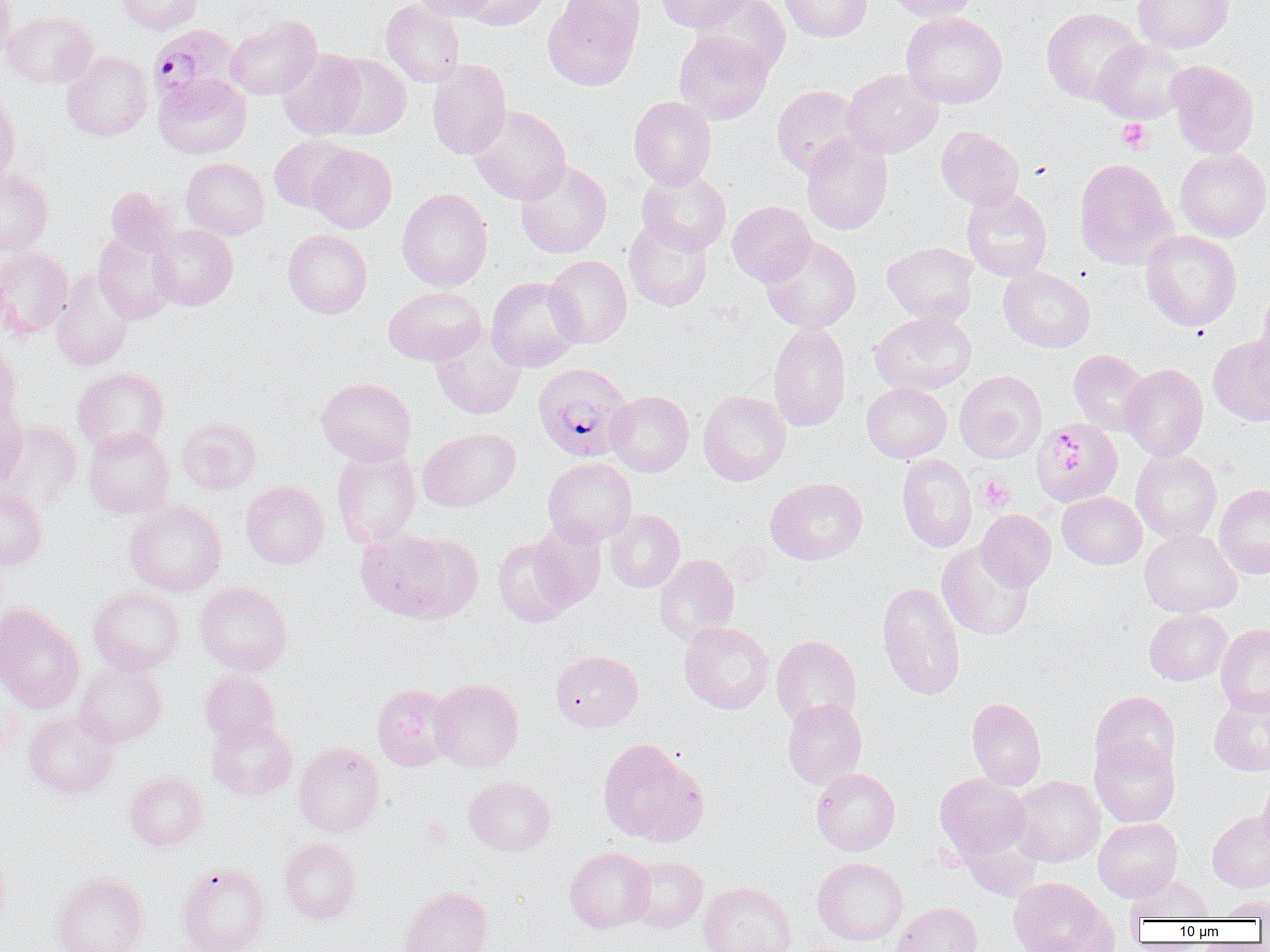

slide-level diagnosis = Plasmodium falciparum
uninfected red blood cell locations = approximate bounding boxes as (x1,y1)-(x2,y2) corner pairs in pixels: (0,0)-(18,66), (116,0)-(202,35), (381,0)-(465,87), (409,0)-(496,20), (460,0)-(550,30), (543,0)-(644,91), (653,0)-(753,32), (694,0)-(790,77), (780,0)-(872,42), (884,0)-(980,22), (1133,0)-(1233,52), (1041,7)-(1146,104), (2,10)-(98,89), (902,11)-(1008,109), (225,15)-(322,100), (674,31)-(773,125), (1093,39)-(1187,124), (277,48)-(366,139), (62,51)-(154,141), (322,53)-(411,139), (427,58)-(511,159), (1166,60)-(1259,158), (841,68)-(943,158), (153,73)-(251,159), (772,85)-(865,177), (0,91)-(20,188), (629,96)-(716,188), (467,104)-(571,204), (936,126)-(1024,209), (801,134)-(893,235), (269,135)-(353,213), (308,144)-(396,233), (1174,147)-(1270,242), (182,158)-(269,240), (1074,158)-(1175,269), (515,161)-(612,258), (0,168)-(53,256), (637,168)-(731,254), (104,186)-(178,257), (397,187)-(493,292), (962,187)-(1052,280), (727,200)-(816,286), (624,218)-(712,311), (149,224)-(238,310), (282,229)-(373,318), (1141,229)-(1241,331), (93,231)-(177,324), (761,235)-(861,333), (883,241)-(978,325), (0,248)-(73,340), (545,255)-(632,348), (998,266)-(1095,352), (50,270)-(135,372), (485,277)-(583,372), (383,286)-(485,366), (1254,288)-(1270,390), (869,311)-(977,395), (768,322)-(851,431), (430,327)-(525,420), (1208,337)-(1270,425), (0,342)-(22,426), (1069,349)-(1152,435), (1120,363)-(1208,461), (72,367)-(169,454), (954,370)-(1046,463), (316,377)-(416,466), (862,382)-(951,462), (607,390)-(694,476), (698,390)-(791,485), (0,396)-(28,488), (177,416)-(261,494), (1032,418)-(1123,507), (1,419)-(83,510), (83,427)-(175,519), (419,427)-(520,511), (331,446)-(421,548), (1131,450)-(1221,543), (897,453)-(977,553), (543,458)-(637,546), (766,477)-(867,565), (241,481)-(329,569), (1214,483)-(1270,579), (0,489)-(47,570), (1057,492)-(1146,569), (124,499)-(226,597), (605,509)-(685,592), (975,509)-(1056,590), (530,525)-(607,611), (355,528)-(467,621), (1139,529)-(1241,616), (493,535)-(583,627), (937,542)-(1034,640), (654,554)-(740,645), (195,581)-(293,675), (876,581)-(966,700), (88,587)-(185,674), (0,603)-(85,713), (1145,608)-(1232,685), (678,621)-(774,714), (1215,623)-(1270,715), (771,634)-(861,727), (550,650)-(643,731), (73,659)-(167,747), (200,670)-(281,747), (429,678)-(524,772), (372,683)-(455,771), (1091,691)-(1180,776), (1209,693)-(1270,776), (966,697)-(1046,791), (782,698)-(867,789), (23,711)-(120,799), (207,718)-(298,800), (1090,736)-(1180,828), (597,737)-(707,846), (294,741)-(385,836), (811,767)-(900,855), (123,771)-(208,851), (935,773)-(1031,863), (1010,775)-(1106,867), (1257,775)-(1270,857), (464,776)-(556,855), (1207,810)-(1270,892), (1093,818)-(1182,901), (280,838)-(361,923), (0,845)-(9,928), (565,846)-(655,932), (627,856)-(708,931), (813,857)-(908,945), (176,863)-(271,952), (50,872)-(149,952), (1126,874)-(1214,922), (1008,876)-(1116,952), (699,881)-(795,952), (398,886)-(493,952), (1215,895)-(1270,920), (892,902)-(982,952)
Plasmodium falciparum-infected red blood cell locations = approximate bounding boxes as (x1,y1)-(x2,y2) corner pairs in pixels: (147,24)-(242,106), (532,363)-(633,462)
platelet locations = approximate bounding boxes as (x1,y1)-(x2,y2) corner pairs in pixels: (1117,118)-(1153,154), (977,475)-(1015,512)
image size = 1270×952 pixels
magnification = 1000x
modality = optical microscopy
field of view = one of a larger specimen
preparation = thin blood film